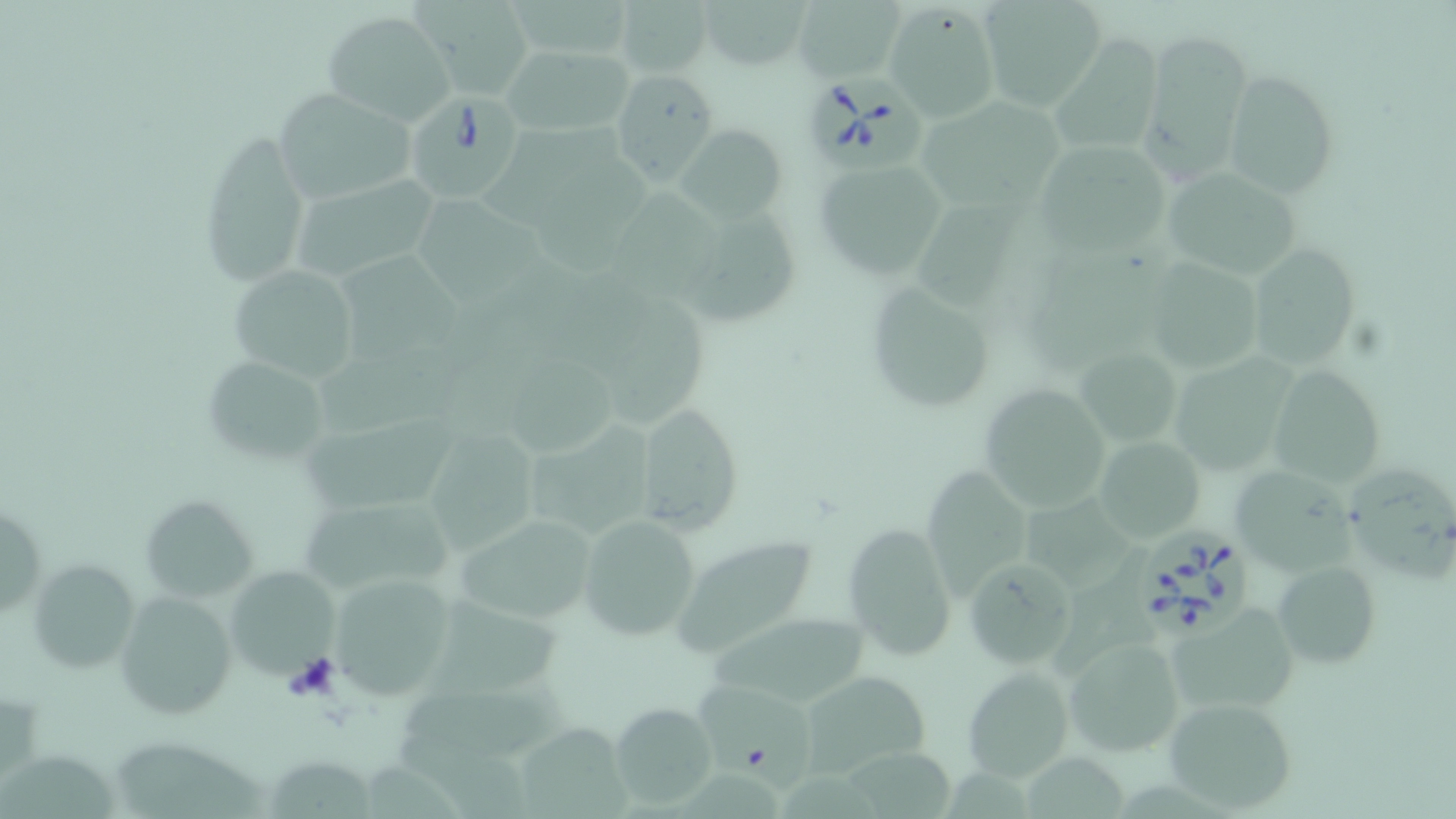
slide-level diagnosis = Babesia divergens
uninfected red blood cell locations = approximate bounding boxes as (x1,y1)-(x2,y2) corner pairs in pixels: (980,0)-(1103,111), (420,1)-(534,99), (615,1)-(713,80), (701,1)-(809,73), (795,1)-(902,81), (884,4)-(997,120), (322,12)-(454,125), (1136,30)-(1251,183), (1054,33)-(1165,153), (503,44)-(633,138), (1223,69)-(1340,197), (611,70)-(718,184), (270,88)-(419,201), (918,94)-(1073,209), (484,124)-(622,230), (680,127)-(788,221), (195,128)-(313,292), (1032,138)-(1173,260), (813,161)-(950,278), (538,162)-(659,278), (1160,167)-(1298,280), (296,174)-(440,277), (613,188)-(724,306), (917,196)-(1032,308), (417,200)-(546,313), (697,207)-(800,325), (1245,245)-(1357,368), (339,254)-(469,365), (1143,258)-(1264,376), (227,266)-(359,380), (858,278)-(997,414), (609,289)-(714,432), (1075,349)-(1182,443), (316,355)-(465,431), (1170,356)-(1291,474), (202,357)-(332,466), (505,358)-(622,462), (1264,363)-(1388,489), (979,381)-(1112,511), (632,401)-(743,534), (299,413)-(456,511), (530,415)-(654,540), (429,424)-(549,554), (1097,435)-(1206,544), (923,462)-(1040,599), (1230,462)-(1357,573), (1347,468)-(1455,587), (1028,491)-(1135,593), (140,495)-(258,598), (303,508)-(463,590), (451,512)-(601,626), (576,513)-(703,641), (0,514)-(41,615), (843,523)-(958,662), (671,537)-(818,660), (1054,545)-(1155,676), (964,558)-(1078,667), (33,559)-(140,669), (1275,561)-(1383,665), (224,564)-(341,680), (327,577)-(455,701), (113,591)-(237,720), (428,596)-(567,703), (1167,602)-(1301,714), (710,613)-(871,707), (1064,634)-(1185,756), (960,667)-(1074,783), (798,670)-(929,777), (693,682)-(814,793), (402,684)-(575,759), (1160,696)-(1298,813), (611,703)-(717,807), (519,720)-(636,819), (395,734)-(532,819), (115,743)-(266,819), (1029,746)-(1125,819), (849,747)-(950,819), (0,754)-(117,817), (268,757)-(371,819), (367,758)-(462,819), (681,767)-(783,819), (947,772)-(1025,819), (778,773)-(881,819)
field of view = single
platelet locations = approximate bounding boxes as (x1,y1)-(x2,y2) corner pairs in pixels: (284,655)-(341,702)
magnification = 1000x
preparation = thin blood film
modality = light microscopy
Babesia divergens-infected red blood cell locations = approximate bounding boxes as (x1,y1)-(x2,y2) corner pairs in pixels: (804,67)-(929,169), (408,97)-(528,204), (1139,527)-(1252,636)
stain = May-Grünwald-Giemsa
image size = 1456×819 pixels